State which parasite is depicted.
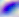

Toxoplasma gondii.

modality: micrograph
magnification: 400x